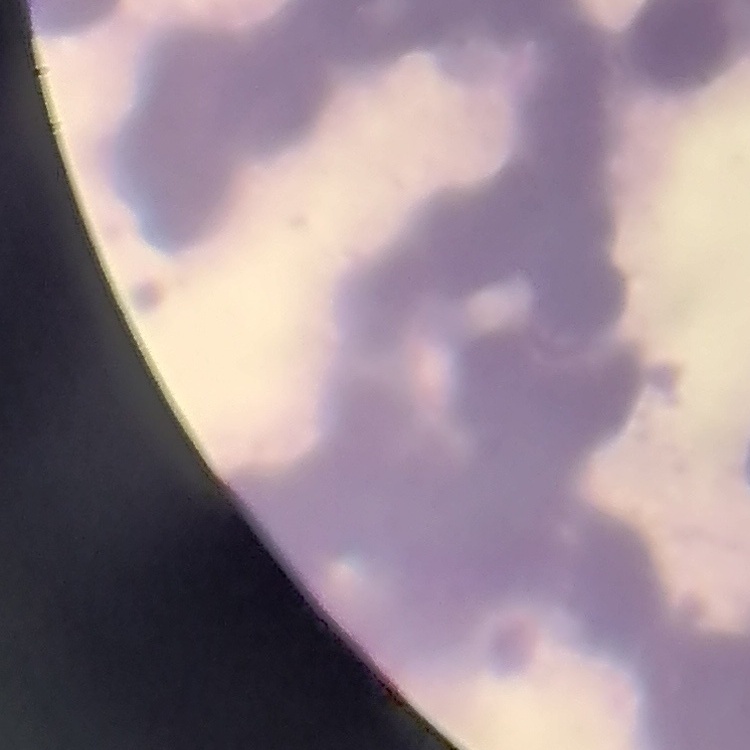
The erythrocytes exhibit rouleaux formation. Stained with either Field's or Giemsa. Square crop of a larger photomicrograph. Thin peripheral smear.